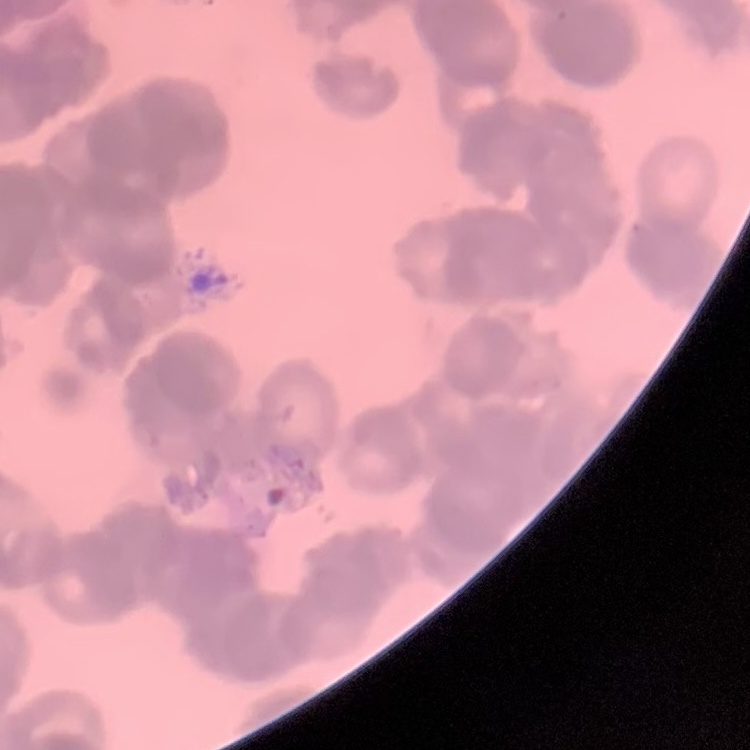
The red blood cells exhibit rouleaux formation. Field's or Giemsa stain. Thin blood smear. Square crop of a larger photomicrograph.